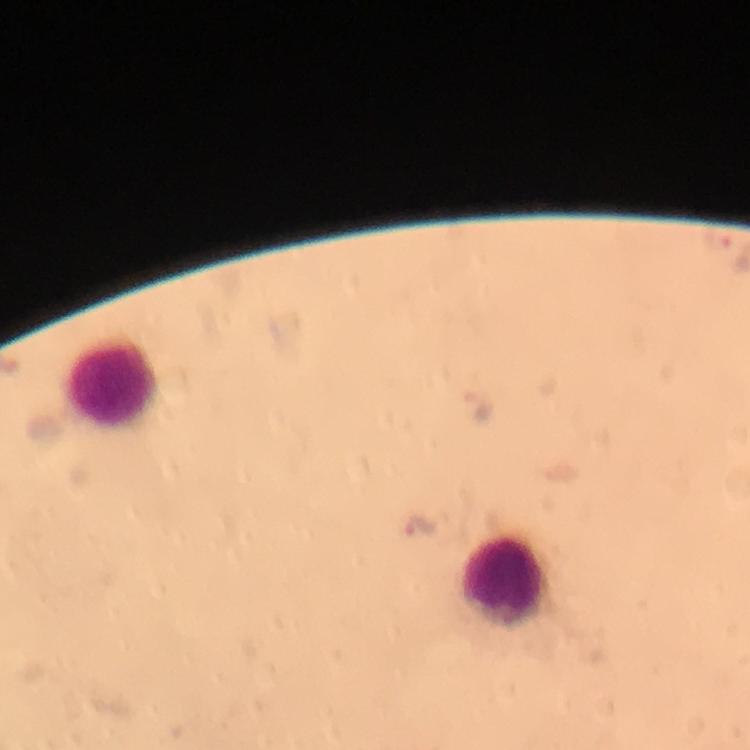

plasmodium_parasite_locations: 'approximate centers as [x, y] in pixels: [476, 402], [423, 525]'
capture: smartphone photograph through a microscope
image_size: 750×750 pixels
stain: Giemsa
leukocyte_locations: 'approximate centers as [x, y] in pixels: [112, 385], [503, 580]'
context: from a malaria diagnostic workup
cropped_from: a single field of view
immersion_oil: applied
preparation: thick blood smear
magnification: 100x